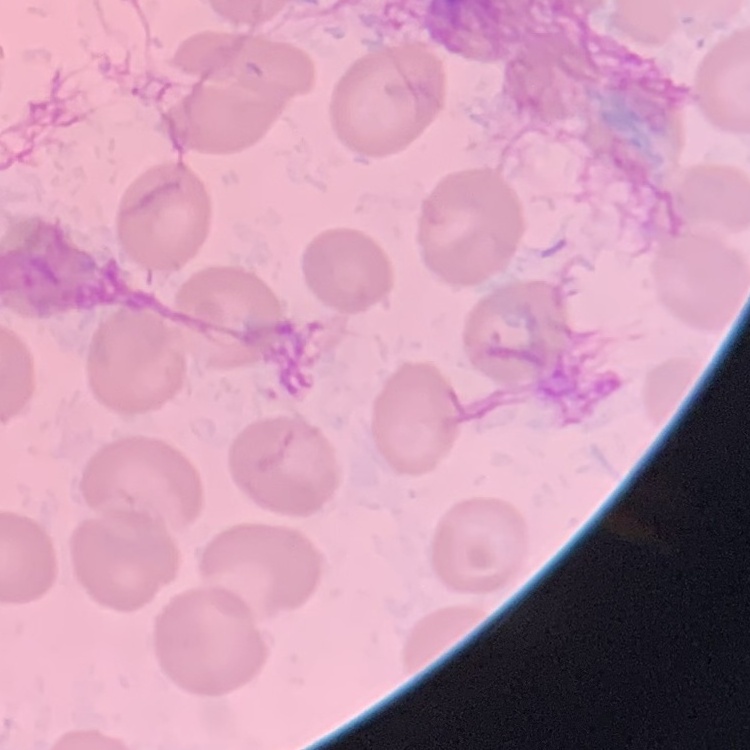 The red blood cells show no rouleaux formation. One tile cut from a larger photomicrograph. Thin blood film. Stained with either Field's or Giemsa.